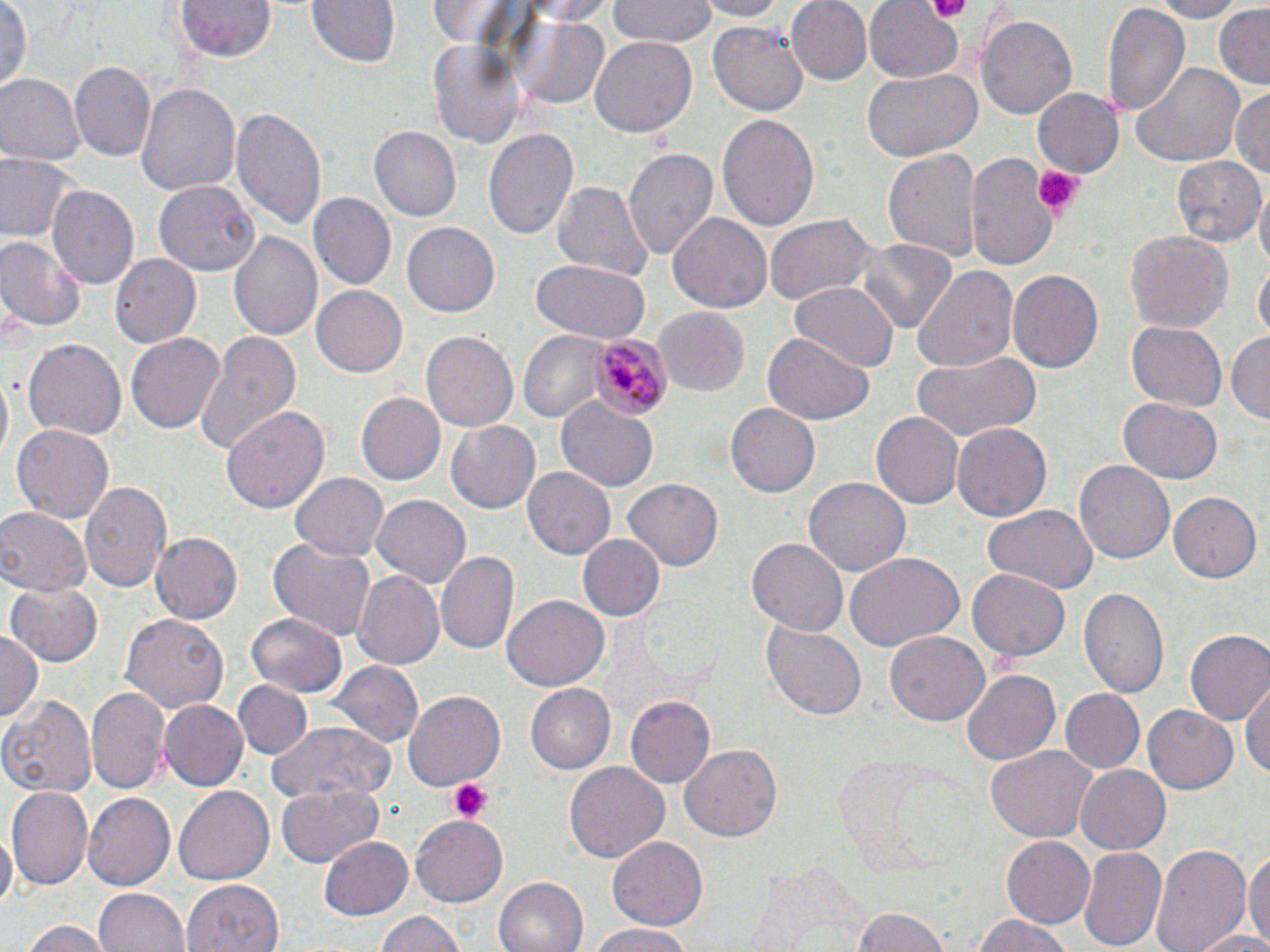 Approximate bounding boxes as named x1/y1/x2/y2 corners in pixels. Plasmodium malariae-infected red blood cell locations: (x1=587, y1=333, x2=671, y2=423). Uninfected red blood cell locations: (x1=175, y1=0, x2=276, y2=61), (x1=306, y1=0, x2=401, y2=69), (x1=511, y1=0, x2=621, y2=24), (x1=696, y1=0, x2=786, y2=21), (x1=787, y1=0, x2=873, y2=85), (x1=864, y1=0, x2=964, y2=82), (x1=1147, y1=0, x2=1246, y2=22), (x1=607, y1=1, x2=720, y2=46), (x1=425, y1=2, x2=532, y2=51), (x1=0, y1=3, x2=32, y2=94), (x1=1101, y1=5, x2=1188, y2=116), (x1=1213, y1=5, x2=1270, y2=85), (x1=513, y1=13, x2=611, y2=110), (x1=978, y1=13, x2=1076, y2=117), (x1=710, y1=19, x2=810, y2=116), (x1=425, y1=34, x2=526, y2=151), (x1=589, y1=37, x2=696, y2=138), (x1=70, y1=60, x2=154, y2=161), (x1=1128, y1=60, x2=1243, y2=168), (x1=863, y1=68, x2=982, y2=161), (x1=0, y1=75, x2=82, y2=167), (x1=136, y1=82, x2=241, y2=199), (x1=1030, y1=86, x2=1123, y2=180), (x1=1231, y1=87, x2=1269, y2=184), (x1=232, y1=107, x2=328, y2=235), (x1=717, y1=111, x2=819, y2=234), (x1=371, y1=127, x2=461, y2=221), (x1=484, y1=128, x2=579, y2=244), (x1=624, y1=145, x2=718, y2=263), (x1=882, y1=147, x2=981, y2=265), (x1=967, y1=152, x2=1060, y2=274), (x1=2, y1=153, x2=74, y2=243), (x1=1171, y1=157, x2=1265, y2=250), (x1=155, y1=179, x2=258, y2=275), (x1=551, y1=180, x2=654, y2=285), (x1=48, y1=184, x2=139, y2=288), (x1=1256, y1=189, x2=1270, y2=278), (x1=310, y1=192, x2=395, y2=290), (x1=670, y1=213, x2=772, y2=314), (x1=765, y1=213, x2=879, y2=307), (x1=402, y1=220, x2=499, y2=314), (x1=1124, y1=229, x2=1233, y2=335), (x1=229, y1=230, x2=322, y2=343), (x1=0, y1=235, x2=86, y2=331), (x1=855, y1=238, x2=957, y2=333), (x1=110, y1=252, x2=201, y2=345), (x1=530, y1=261, x2=650, y2=343), (x1=1254, y1=262, x2=1269, y2=344), (x1=913, y1=264, x2=1018, y2=371), (x1=1008, y1=268, x2=1104, y2=373), (x1=791, y1=283, x2=896, y2=373), (x1=311, y1=287, x2=406, y2=377), (x1=654, y1=308, x2=750, y2=396), (x1=1126, y1=321, x2=1227, y2=412), (x1=421, y1=328, x2=518, y2=429), (x1=194, y1=331, x2=304, y2=455), (x1=519, y1=331, x2=609, y2=421), (x1=1227, y1=331, x2=1270, y2=428), (x1=126, y1=333, x2=225, y2=435), (x1=760, y1=334, x2=875, y2=425), (x1=23, y1=338, x2=125, y2=442), (x1=910, y1=351, x2=1041, y2=445), (x1=358, y1=391, x2=444, y2=483), (x1=556, y1=397, x2=660, y2=491), (x1=1116, y1=397, x2=1223, y2=484), (x1=725, y1=403, x2=819, y2=498), (x1=221, y1=404, x2=329, y2=517), (x1=871, y1=412, x2=962, y2=509), (x1=447, y1=418, x2=543, y2=514), (x1=10, y1=423, x2=114, y2=525), (x1=951, y1=423, x2=1053, y2=522), (x1=1074, y1=458, x2=1176, y2=564), (x1=523, y1=466, x2=617, y2=557), (x1=291, y1=473, x2=387, y2=561), (x1=624, y1=476, x2=722, y2=569), (x1=803, y1=477, x2=912, y2=579), (x1=79, y1=481, x2=174, y2=596), (x1=1169, y1=491, x2=1259, y2=581), (x1=372, y1=493, x2=471, y2=588), (x1=0, y1=507, x2=91, y2=595), (x1=981, y1=507, x2=1096, y2=597), (x1=150, y1=531, x2=243, y2=623), (x1=580, y1=533, x2=663, y2=622), (x1=747, y1=536, x2=848, y2=636), (x1=268, y1=539, x2=375, y2=644), (x1=437, y1=548, x2=517, y2=654), (x1=846, y1=554, x2=965, y2=651), (x1=968, y1=568, x2=1070, y2=662), (x1=353, y1=572, x2=445, y2=669), (x1=5, y1=582, x2=104, y2=667), (x1=1080, y1=584, x2=1170, y2=702), (x1=504, y1=594, x2=609, y2=690), (x1=247, y1=611, x2=346, y2=696), (x1=121, y1=614, x2=230, y2=714), (x1=763, y1=622, x2=867, y2=721), (x1=1185, y1=630, x2=1270, y2=728), (x1=0, y1=631, x2=41, y2=726), (x1=885, y1=633, x2=988, y2=724), (x1=332, y1=661, x2=422, y2=748), (x1=960, y1=669, x2=1061, y2=765), (x1=235, y1=680, x2=310, y2=760), (x1=1242, y1=682, x2=1269, y2=784), (x1=523, y1=683, x2=615, y2=773), (x1=86, y1=685, x2=168, y2=792), (x1=1059, y1=688, x2=1144, y2=774), (x1=402, y1=692, x2=504, y2=793), (x1=627, y1=695, x2=717, y2=789), (x1=1, y1=698, x2=97, y2=797), (x1=158, y1=702, x2=247, y2=789), (x1=1144, y1=702, x2=1240, y2=795), (x1=268, y1=720, x2=398, y2=805), (x1=679, y1=742, x2=783, y2=843), (x1=983, y1=744, x2=1097, y2=844), (x1=565, y1=761, x2=670, y2=864), (x1=1074, y1=764, x2=1170, y2=853), (x1=276, y1=784, x2=386, y2=867), (x1=174, y1=785, x2=275, y2=886), (x1=9, y1=786, x2=92, y2=890), (x1=83, y1=793, x2=175, y2=890), (x1=411, y1=813, x2=510, y2=908), (x1=0, y1=828, x2=15, y2=913), (x1=320, y1=833, x2=416, y2=921), (x1=608, y1=835, x2=708, y2=930), (x1=999, y1=835, x2=1096, y2=928), (x1=1151, y1=841, x2=1251, y2=952), (x1=1077, y1=845, x2=1166, y2=952), (x1=1243, y1=847, x2=1270, y2=952), (x1=492, y1=875, x2=589, y2=952), (x1=183, y1=878, x2=283, y2=952), (x1=93, y1=888, x2=189, y2=952), (x1=847, y1=907, x2=951, y2=951), (x1=372, y1=910, x2=472, y2=952), (x1=971, y1=913, x2=1078, y2=952), (x1=22, y1=919, x2=114, y2=952), (x1=584, y1=922, x2=700, y2=952), (x1=1188, y1=930, x2=1270, y2=952). Platelet locations: (x1=925, y1=0, x2=974, y2=21), (x1=1033, y1=166, x2=1079, y2=217), (x1=446, y1=779, x2=490, y2=822). Slide-level diagnosis: Plasmodium malariae. Image is 1270×952 pixels. May-Grünwald-Giemsa stain. One field of a larger specimen. Optical microscopy. Captured at 1000x magnification. Thin blood film.